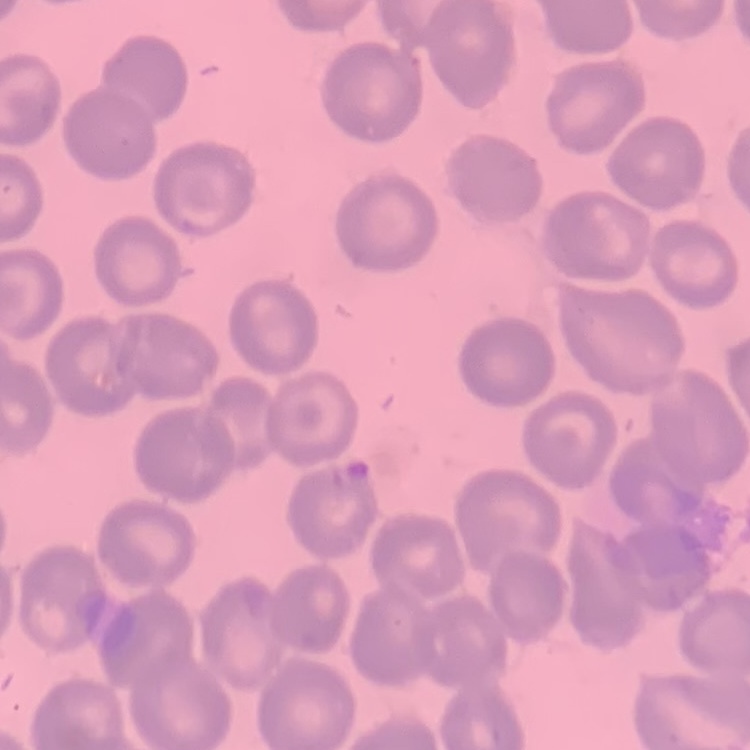

red_blood_cell_morphology: no rouleaux formation
stain: Field's or Giemsa
image_type: one tile cut from a larger photomicrograph
preparation: thin peripheral smear